Locate and identify every blood parasite.
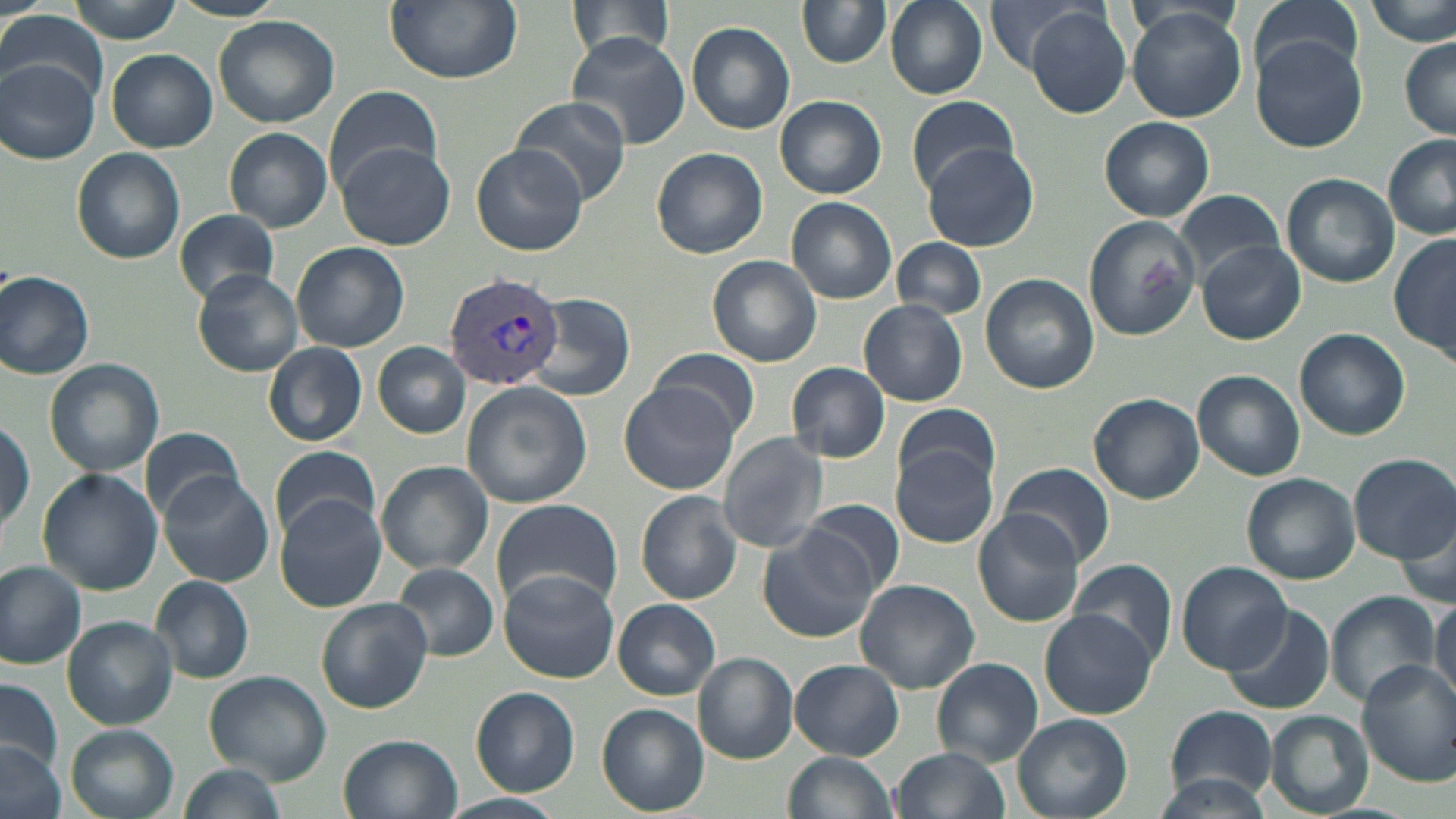

Approximate bounding boxes as named x1/y1/x2/y2 corners in pixels.
Plasmodium vivax-infected red blood cells: (x1=442, y1=270, x2=564, y2=391).
No Plasmodium falciparum, Plasmodium ovale, Plasmodium malariae, Babesia divergens, or Trypanosoma brucei observed.

Uninfected red blood cell locations: (x1=66, y1=0, x2=185, y2=42), (x1=167, y1=0, x2=286, y2=21), (x1=383, y1=0, x2=521, y2=84), (x1=564, y1=0, x2=679, y2=64), (x1=796, y1=0, x2=892, y2=68), (x1=885, y1=0, x2=987, y2=98), (x1=984, y1=0, x2=1098, y2=74), (x1=1248, y1=0, x2=1364, y2=86), (x1=1369, y1=0, x2=1455, y2=48), (x1=1027, y1=6, x2=1131, y2=119), (x1=1125, y1=8, x2=1249, y2=122), (x1=1, y1=11, x2=107, y2=100), (x1=213, y1=16, x2=340, y2=127), (x1=685, y1=21, x2=795, y2=134), (x1=566, y1=32, x2=691, y2=149), (x1=1250, y1=36, x2=1368, y2=152), (x1=1401, y1=41, x2=1455, y2=137), (x1=107, y1=49, x2=217, y2=152), (x1=2, y1=58, x2=99, y2=164), (x1=325, y1=83, x2=443, y2=196), (x1=906, y1=94, x2=1018, y2=193), (x1=775, y1=95, x2=886, y2=198), (x1=512, y1=99, x2=630, y2=204), (x1=1099, y1=116, x2=1214, y2=219), (x1=224, y1=127, x2=333, y2=232), (x1=1381, y1=133, x2=1456, y2=236), (x1=336, y1=141, x2=456, y2=250), (x1=471, y1=142, x2=589, y2=257), (x1=923, y1=144, x2=1042, y2=252), (x1=72, y1=146, x2=186, y2=264), (x1=651, y1=146, x2=768, y2=258), (x1=1281, y1=173, x2=1399, y2=287), (x1=1172, y1=189, x2=1288, y2=283), (x1=786, y1=197, x2=897, y2=304), (x1=172, y1=208, x2=279, y2=305), (x1=1082, y1=215, x2=1202, y2=341), (x1=1389, y1=233, x2=1455, y2=365), (x1=893, y1=238, x2=987, y2=320), (x1=1194, y1=239, x2=1306, y2=345), (x1=292, y1=242, x2=410, y2=353), (x1=707, y1=255, x2=822, y2=367), (x1=0, y1=269, x2=95, y2=380), (x1=192, y1=270, x2=302, y2=376), (x1=980, y1=273, x2=1099, y2=393), (x1=526, y1=292, x2=638, y2=402), (x1=860, y1=300, x2=967, y2=405), (x1=1293, y1=328, x2=1411, y2=440), (x1=374, y1=342, x2=470, y2=438), (x1=264, y1=343, x2=367, y2=446), (x1=652, y1=347, x2=759, y2=438), (x1=43, y1=358, x2=164, y2=477), (x1=786, y1=362, x2=891, y2=463), (x1=1193, y1=369, x2=1304, y2=481), (x1=462, y1=381, x2=591, y2=508), (x1=619, y1=383, x2=740, y2=495), (x1=1090, y1=393, x2=1204, y2=504), (x1=892, y1=401, x2=1003, y2=498), (x1=1, y1=415, x2=33, y2=538), (x1=137, y1=425, x2=242, y2=523), (x1=717, y1=433, x2=830, y2=551), (x1=269, y1=446, x2=382, y2=541), (x1=892, y1=446, x2=998, y2=548), (x1=1348, y1=453, x2=1456, y2=562), (x1=374, y1=460, x2=493, y2=575), (x1=1000, y1=462, x2=1115, y2=568), (x1=37, y1=468, x2=162, y2=595), (x1=158, y1=470, x2=274, y2=586), (x1=1242, y1=473, x2=1359, y2=583), (x1=636, y1=490, x2=741, y2=603), (x1=275, y1=492, x2=391, y2=615), (x1=800, y1=498, x2=905, y2=595), (x1=490, y1=499, x2=621, y2=611), (x1=1398, y1=509, x2=1455, y2=610), (x1=972, y1=511, x2=1085, y2=626), (x1=756, y1=530, x2=882, y2=643), (x1=1069, y1=558, x2=1177, y2=665), (x1=0, y1=561, x2=88, y2=667), (x1=392, y1=562, x2=499, y2=661), (x1=1177, y1=562, x2=1289, y2=673), (x1=498, y1=571, x2=619, y2=683), (x1=151, y1=577, x2=254, y2=684), (x1=855, y1=579, x2=980, y2=693), (x1=1325, y1=591, x2=1441, y2=707), (x1=1431, y1=596, x2=1455, y2=705), (x1=316, y1=597, x2=433, y2=712), (x1=613, y1=599, x2=721, y2=700), (x1=1220, y1=605, x2=1337, y2=716), (x1=1039, y1=609, x2=1159, y2=720), (x1=64, y1=617, x2=176, y2=728), (x1=695, y1=652, x2=798, y2=763), (x1=930, y1=657, x2=1043, y2=766), (x1=791, y1=660, x2=903, y2=759), (x1=1356, y1=660, x2=1456, y2=784), (x1=203, y1=669, x2=332, y2=784), (x1=1, y1=677, x2=64, y2=777), (x1=471, y1=686, x2=580, y2=796), (x1=598, y1=704, x2=708, y2=816), (x1=1164, y1=706, x2=1279, y2=801), (x1=1265, y1=710, x2=1374, y2=817), (x1=1012, y1=713, x2=1131, y2=819), (x1=64, y1=724, x2=180, y2=819), (x1=339, y1=734, x2=463, y2=819), (x1=0, y1=742, x2=65, y2=819), (x1=892, y1=748, x2=1009, y2=819), (x1=783, y1=752, x2=899, y2=819), (x1=178, y1=763, x2=288, y2=817), (x1=1149, y1=775, x2=1277, y2=819), (x1=439, y1=793, x2=569, y2=819). Slide-level diagnosis: Plasmodium vivax. May-Grünwald-Giemsa-stained preparation. Image is 1456×819 pixels. Light microscopy. Thin blood film. 1000x magnification. One field of a larger specimen.